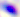
Summary:
  - Modality: micrograph
  - Identification: Toxoplasma gondii
  - Magnification: 400x